Evaluate for malaria.
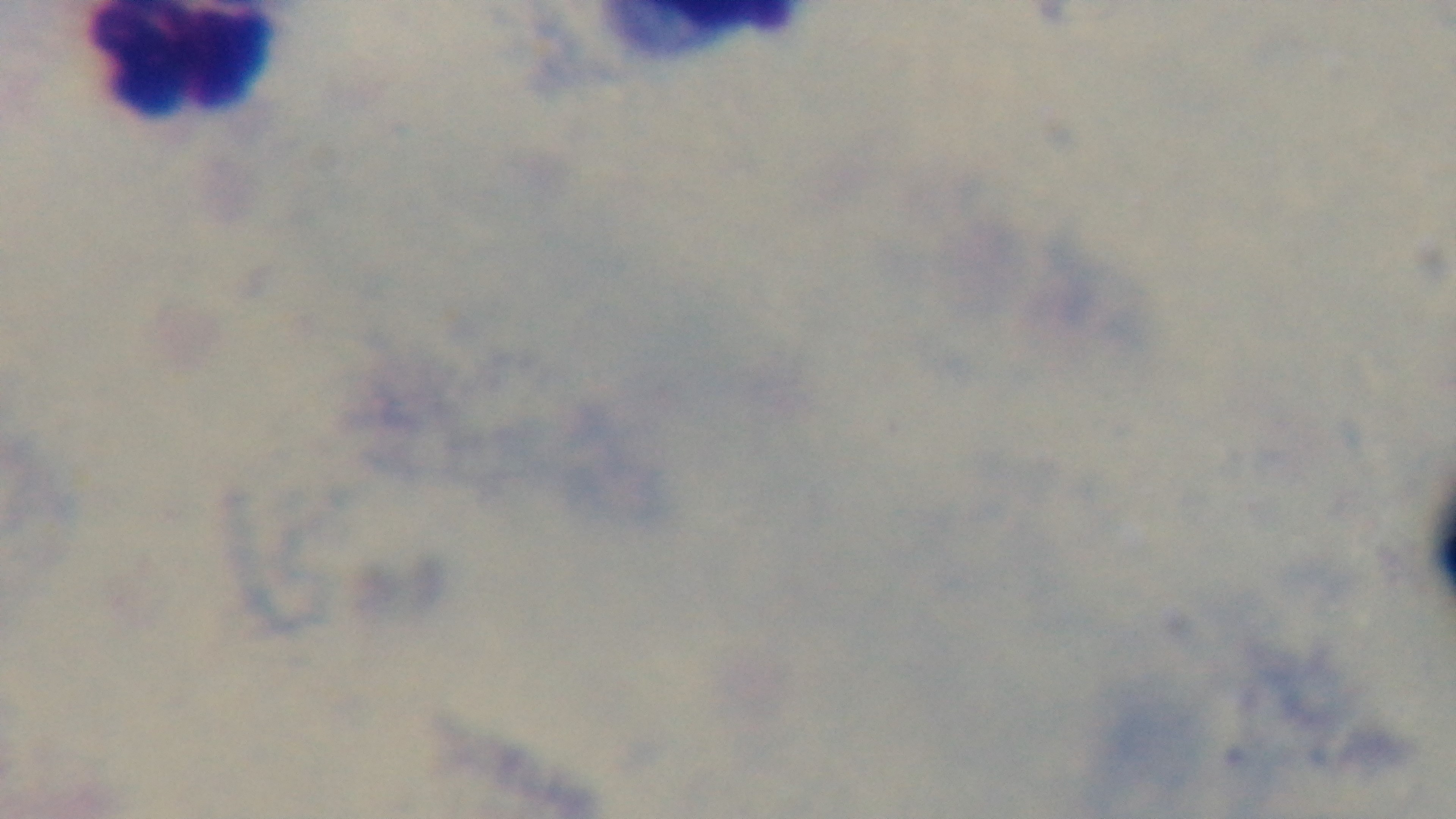
It is uninfected.

field_of_view: one from the slide
stain: Giemsa
objective: 100x oil immersion
modality: light microscopy
preparation: thick
capture: mounted 4K digital camera